Locate every blood parasite and identify its species.
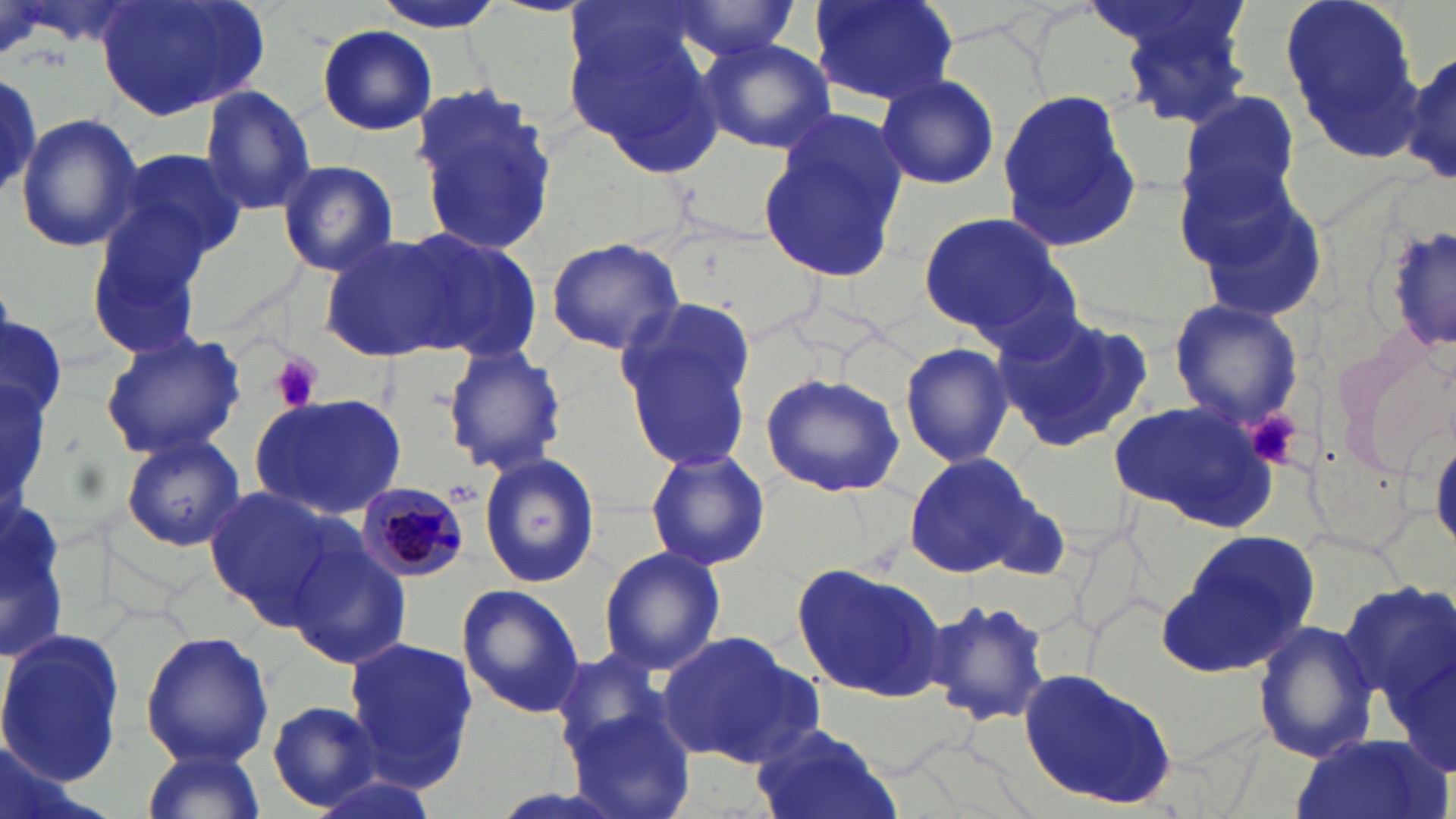

Approximate bounding boxes as (x1,y1)-(x2,y2) corner pairs in pixels.
Plasmodium malariae-infected red blood cells: (357,481)-(470,581).
No Plasmodium falciparum, Plasmodium ovale, Plasmodium vivax, Babesia divergens, or Trypanosoma brucei observed.

Summary:
  - Uninfected red blood cell locations: (94,0)-(267,123), (374,0)-(509,33), (811,0)-(957,105), (1100,0)-(1258,128), (1278,0)-(1426,163), (562,1)-(734,173), (664,2)-(804,62), (316,22)-(439,134), (697,38)-(835,153), (1397,48)-(1456,188), (874,72)-(1000,191), (408,82)-(559,261), (197,86)-(318,213), (996,89)-(1143,250), (1174,91)-(1305,227), (16,114)-(144,253), (758,114)-(907,286), (108,147)-(249,265), (277,159)-(399,275), (1177,167)-(1329,324), (84,208)-(218,359), (917,208)-(1075,340), (318,233)-(470,362), (407,234)-(545,363), (544,239)-(687,355), (614,297)-(756,471), (1167,299)-(1305,429), (997,309)-(1155,451), (98,329)-(247,461), (1330,335)-(1456,475), (898,342)-(1016,467), (441,345)-(567,475), (758,370)-(908,499), (251,391)-(409,521), (1106,399)-(1279,530), (119,433)-(245,552), (1430,433)-(1456,553), (3,438)-(74,684), (644,447)-(771,574), (903,452)-(1035,577), (480,454)-(599,588), (204,485)-(351,630), (977,488)-(1074,582), (1162,528)-(1321,676), (285,534)-(413,673), (598,546)-(727,677), (791,561)-(948,703), (1339,581)-(1455,711), (456,584)-(585,720), (921,596)-(1056,729), (1251,619)-(1380,765), (0,630)-(126,789), (656,630)-(823,766), (140,631)-(273,767), (1385,635)-(1456,780), (342,638)-(478,786), (551,647)-(682,767), (1019,665)-(1182,811), (266,702)-(384,812), (562,707)-(697,819), (751,723)-(899,819), (1289,735)-(1451,819), (138,745)-(267,819)
  - Platelet locations: (271,355)-(321,412), (1249,408)-(1304,470)
  - Slide-level diagnosis: Plasmodium malariae
  - Magnification: 1000x
  - Stain: May-Grünwald-Giemsa
  - Preparation: thin blood smear
  - Modality: light microscopy
  - Field of view: single
  - Image size: 1456×819 pixels